Assess this cell for malaria.
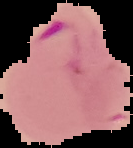
Parasitized.

From a thin blood film. Image is 133×148 pixels. Cell region segmented out of the field of view; the surrounding area is masked to black.